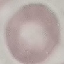
Result: no malaria parasites seen. Cell patch, automatically extracted from a larger field of view and resized to 64 × 64 pixels. Giemsa-stained preparation. Thin blood film. Acquired by smartphone through the microscope eyepiece.